Point out each Plasmodium parasite and classify it by life-cycle stage.
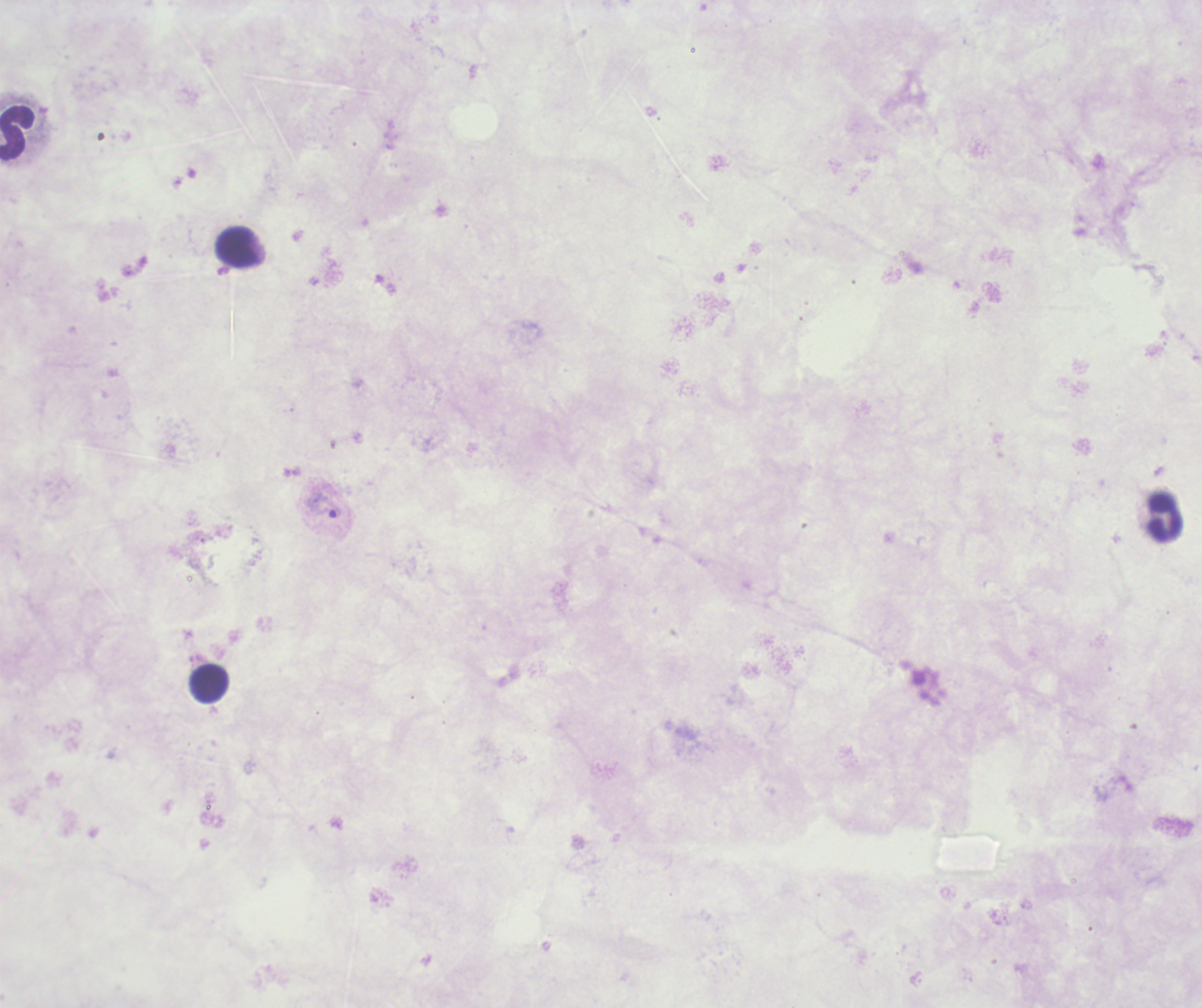

Approximate object centers, in pixels from the top-left corner.
Trophozoites: (x=324, y=506).
No schizont or gametocyte forms observed.

Approximate object centers, in pixels from the top-left corner. Leukocyte locations: (x=17, y=133), (x=238, y=248), (x=1166, y=517), (x=209, y=683). One field from this slide. Previously used in an actual diagnosis. Background quality: poor. Thick smear of blood. Coloration quality: bad. Romanowsky stain. Image is 1202×1008 pixels. Captured at 100x magnification.